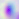
Summary:
  - Modality: micrograph
  - Identification: Toxoplasma gondii
  - Magnification: 400x